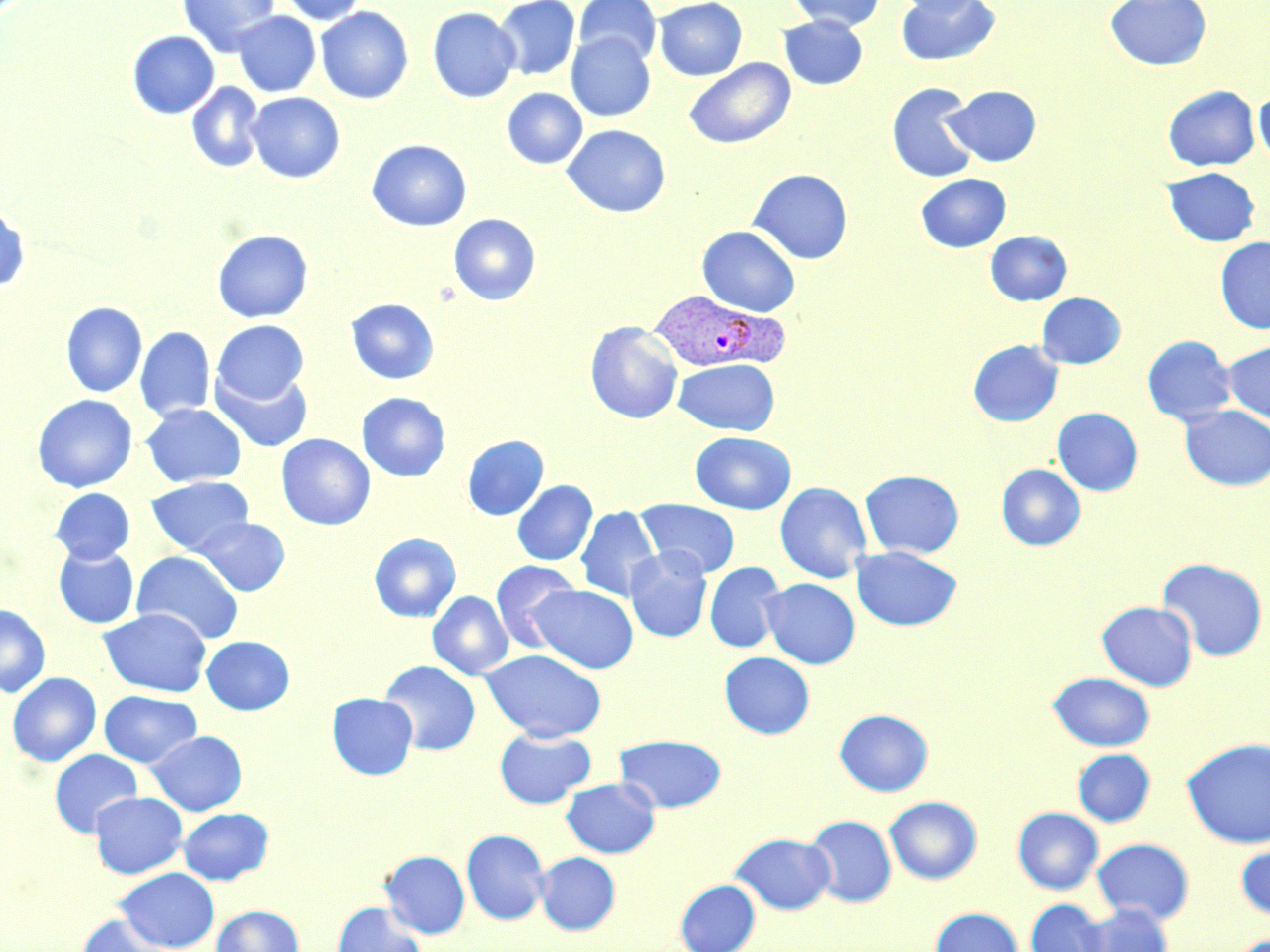
slide-level diagnosis = Plasmodium vivax
image size = 1270×952 pixels
field of view = one of a larger specimen
Plasmodium vivax-infected red blood cell locations = approximate bounding boxes as (x1,y1)-(x2,y2) corner pairs in pixels: (648,291)-(789,374)
stain = May-Grünwald-Giemsa
preparation = thin blood film
uninfected red blood cell locations = approximate bounding boxes as (x1,y1)-(x2,y2) corner pairs in pixels: (177,0)-(280,56), (279,0)-(368,25), (494,0)-(580,81), (573,0)-(662,66), (654,0)-(747,81), (789,0)-(885,31), (891,0)-(988,17), (894,0)-(1001,67), (1105,0)-(1211,71), (315,6)-(414,104), (427,7)-(521,103), (232,11)-(320,97), (778,15)-(868,90), (127,30)-(220,119), (566,32)-(655,122), (684,57)-(795,150), (186,82)-(265,174), (886,82)-(980,183), (944,85)-(1041,167), (1163,85)-(1260,171), (502,88)-(587,169), (1254,89)-(1270,168), (246,92)-(345,183), (562,124)-(671,218), (366,139)-(472,231), (1162,166)-(1261,247), (748,168)-(853,265), (915,173)-(1011,253), (0,205)-(30,291), (449,213)-(540,305), (697,225)-(800,317), (212,229)-(314,323), (985,230)-(1072,306), (1215,236)-(1270,334), (1036,292)-(1126,369), (345,298)-(439,385), (60,301)-(147,398), (212,319)-(309,404), (585,321)-(683,424), (135,326)-(215,422), (1141,334)-(1237,426), (967,340)-(1063,427), (1221,340)-(1270,425), (672,358)-(780,435), (210,366)-(313,453), (356,392)-(450,481), (32,394)-(137,493), (141,403)-(247,488), (1180,405)-(1270,491), (1052,407)-(1143,496), (690,431)-(796,514), (277,433)-(375,530), (462,435)-(549,521), (996,464)-(1086,551), (859,469)-(964,559), (145,476)-(254,556), (511,480)-(597,566), (774,481)-(873,583), (50,488)-(135,564), (636,500)-(740,578), (575,506)-(662,602), (194,517)-(290,596), (369,533)-(461,622), (53,545)-(139,629), (851,545)-(961,631), (625,548)-(712,643), (131,550)-(244,645), (1156,557)-(1268,661), (490,560)-(582,652), (704,561)-(786,653), (760,577)-(860,669), (528,584)-(639,674), (427,590)-(514,680), (1096,601)-(1197,690), (0,604)-(51,698), (98,608)-(212,696), (201,636)-(295,715), (480,649)-(607,742), (719,651)-(814,739), (379,660)-(481,755), (7,672)-(101,766), (1048,672)-(1155,750), (99,690)-(202,768), (327,693)-(418,780), (834,709)-(933,796), (494,728)-(596,809), (146,730)-(247,815), (614,734)-(726,813), (1181,738)-(1270,848), (49,748)-(143,837), (1073,748)-(1156,827), (561,777)-(660,858), (89,791)-(187,879), (884,796)-(982,884), (177,807)-(273,885), (1012,807)-(1104,894), (804,814)-(896,907), (461,829)-(550,925), (731,832)-(835,915), (1092,838)-(1194,924), (1235,842)-(1270,922), (380,850)-(470,939), (534,852)-(620,935), (115,867)-(220,951), (676,879)-(760,952), (1025,898)-(1109,952), (331,901)-(425,951), (1078,903)-(1173,952), (211,904)-(304,952), (929,907)-(1024,952), (75,913)-(176,952)
magnification = 1000x
modality = light microscopy